Assess the background quality.
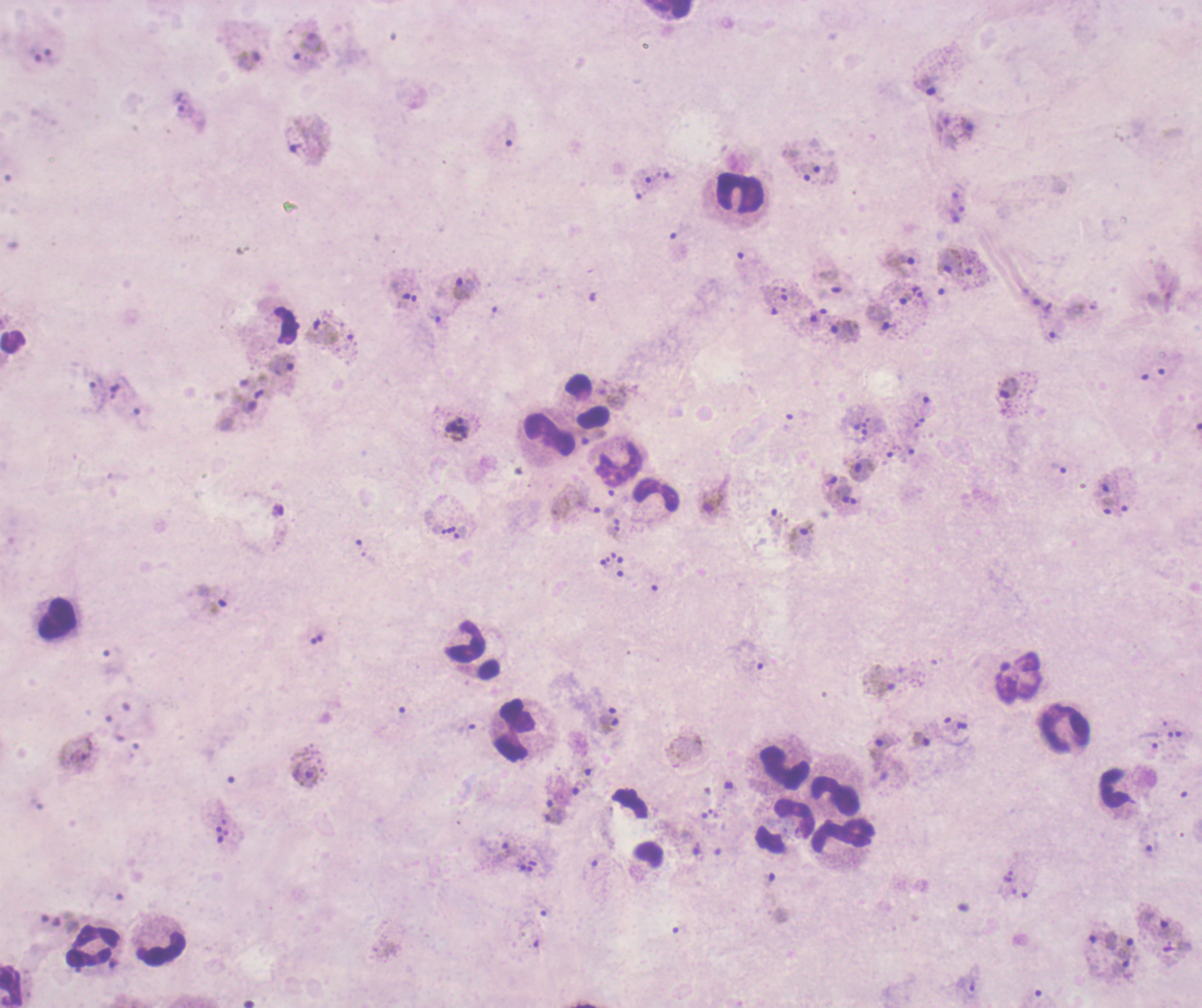

Poor.

coordinate format = approximate centers as (x, y) in pixels
schizont locations = (457, 428)
gametocyte locations = (712, 496), (880, 681), (304, 774)
leukocyte locations = (669, 9), (742, 194), (287, 325), (587, 402), (548, 435), (619, 464), (656, 494), (57, 619), (472, 652), (1064, 728), (515, 731), (784, 768), (1114, 788), (834, 797), (783, 824), (843, 834), (93, 946), (161, 947), (11, 985)
trophozoite locations = (308, 45), (248, 61), (927, 85), (182, 105), (967, 127), (637, 189), (899, 262), (465, 288), (882, 319), (320, 332), (844, 332), (281, 363), (1009, 388), (862, 471), (1104, 484), (575, 501), (799, 541), (608, 725), (950, 727), (920, 740), (1149, 741), (885, 749), (555, 816), (1150, 848), (1008, 877), (1164, 927), (1125, 946), (971, 984)
life-cycle stages observed = trophozoite, schizont, gametocyte
coloration quality = bad
result = Plasmodium parasites detected
image size = 1202×1008 pixels
stain = Romanowsky
magnification = 100x
preparation = thick blood film
field of view = single
context = previously used in a real diagnosis